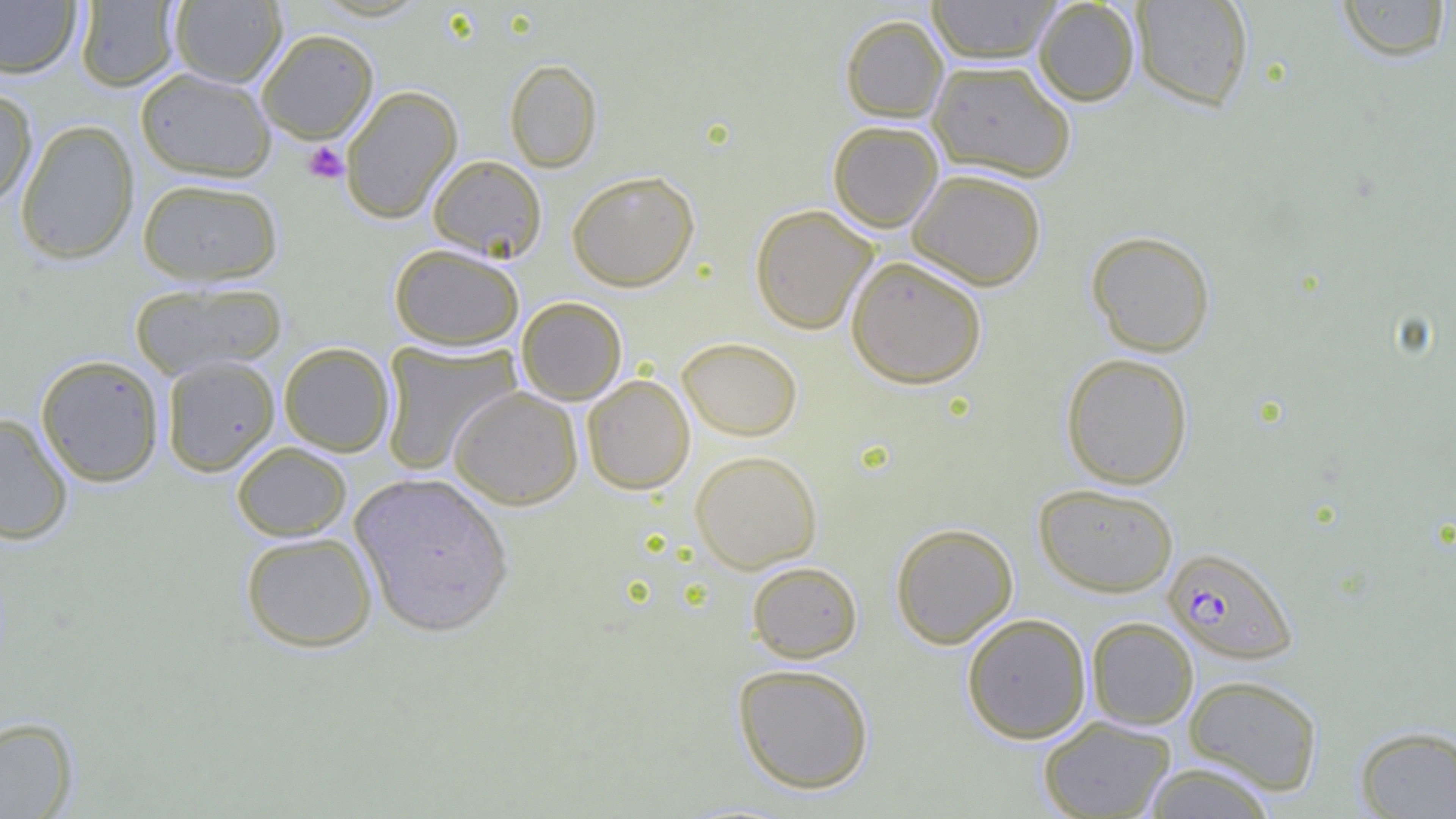

{
  "plasmodium_falciparum_infected_red_blood_cell_locations": "approximate bounding boxes as named x1/y1/x2/y2 corners in pixels: (x1=1163, y1=546, x2=1297, y2=663)",
  "slide_level_diagnosis": "Plasmodium falciparum",
  "preparation": "thin blood smear",
  "field_of_view": "one of a larger specimen",
  "uninfected_red_blood_cell_locations": "approximate bounding boxes as named x1/y1/x2/y2 corners in pixels: (x1=0, y1=0, x2=81, y2=78), (x1=75, y1=0, x2=181, y2=92), (x1=927, y1=0, x2=1061, y2=64), (x1=1033, y1=0, x2=1140, y2=106), (x1=1130, y1=0, x2=1254, y2=111), (x1=1336, y1=0, x2=1452, y2=62), (x1=168, y1=1, x2=287, y2=87), (x1=840, y1=14, x2=949, y2=123), (x1=256, y1=29, x2=379, y2=144), (x1=504, y1=59, x2=602, y2=172), (x1=928, y1=59, x2=1076, y2=181), (x1=135, y1=68, x2=276, y2=182), (x1=340, y1=85, x2=463, y2=224), (x1=0, y1=86, x2=38, y2=210), (x1=15, y1=119, x2=140, y2=265), (x1=827, y1=120, x2=944, y2=232), (x1=427, y1=154, x2=547, y2=262), (x1=907, y1=168, x2=1047, y2=290), (x1=567, y1=170, x2=699, y2=291), (x1=137, y1=178, x2=283, y2=286), (x1=749, y1=204, x2=879, y2=335), (x1=1086, y1=230, x2=1216, y2=357), (x1=389, y1=243, x2=525, y2=350), (x1=845, y1=255, x2=987, y2=389), (x1=129, y1=281, x2=287, y2=378), (x1=516, y1=296, x2=627, y2=405), (x1=677, y1=336, x2=803, y2=440), (x1=379, y1=341, x2=520, y2=474), (x1=279, y1=342, x2=395, y2=456), (x1=1060, y1=352, x2=1194, y2=489), (x1=35, y1=354, x2=165, y2=487), (x1=161, y1=354, x2=280, y2=476), (x1=582, y1=374, x2=695, y2=494), (x1=448, y1=386, x2=583, y2=509), (x1=0, y1=412, x2=74, y2=545), (x1=231, y1=441, x2=352, y2=541), (x1=690, y1=450, x2=822, y2=573), (x1=350, y1=472, x2=514, y2=638), (x1=1033, y1=483, x2=1179, y2=597), (x1=890, y1=522, x2=1018, y2=649), (x1=240, y1=531, x2=378, y2=652), (x1=746, y1=561, x2=863, y2=663), (x1=961, y1=612, x2=1092, y2=744), (x1=1086, y1=616, x2=1198, y2=730), (x1=733, y1=663, x2=874, y2=794), (x1=1183, y1=674, x2=1323, y2=794), (x1=1037, y1=715, x2=1176, y2=819), (x1=0, y1=716, x2=78, y2=818), (x1=1354, y1=724, x2=1456, y2=818), (x1=1140, y1=761, x2=1278, y2=818)",
  "platelet_locations": "approximate bounding boxes as named x1/y1/x2/y2 corners in pixels: (x1=303, y1=141, x2=348, y2=184)",
  "modality": "light microscopy",
  "magnification": "1000x",
  "image_size": "1456×819 pixels"
}